Assess this cell for malaria.
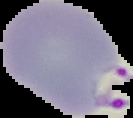

Parasitized.

Cell region segmented out of the field of view; the surrounding area is masked to black. From a thin blood smear. Image is 133×118 pixels.